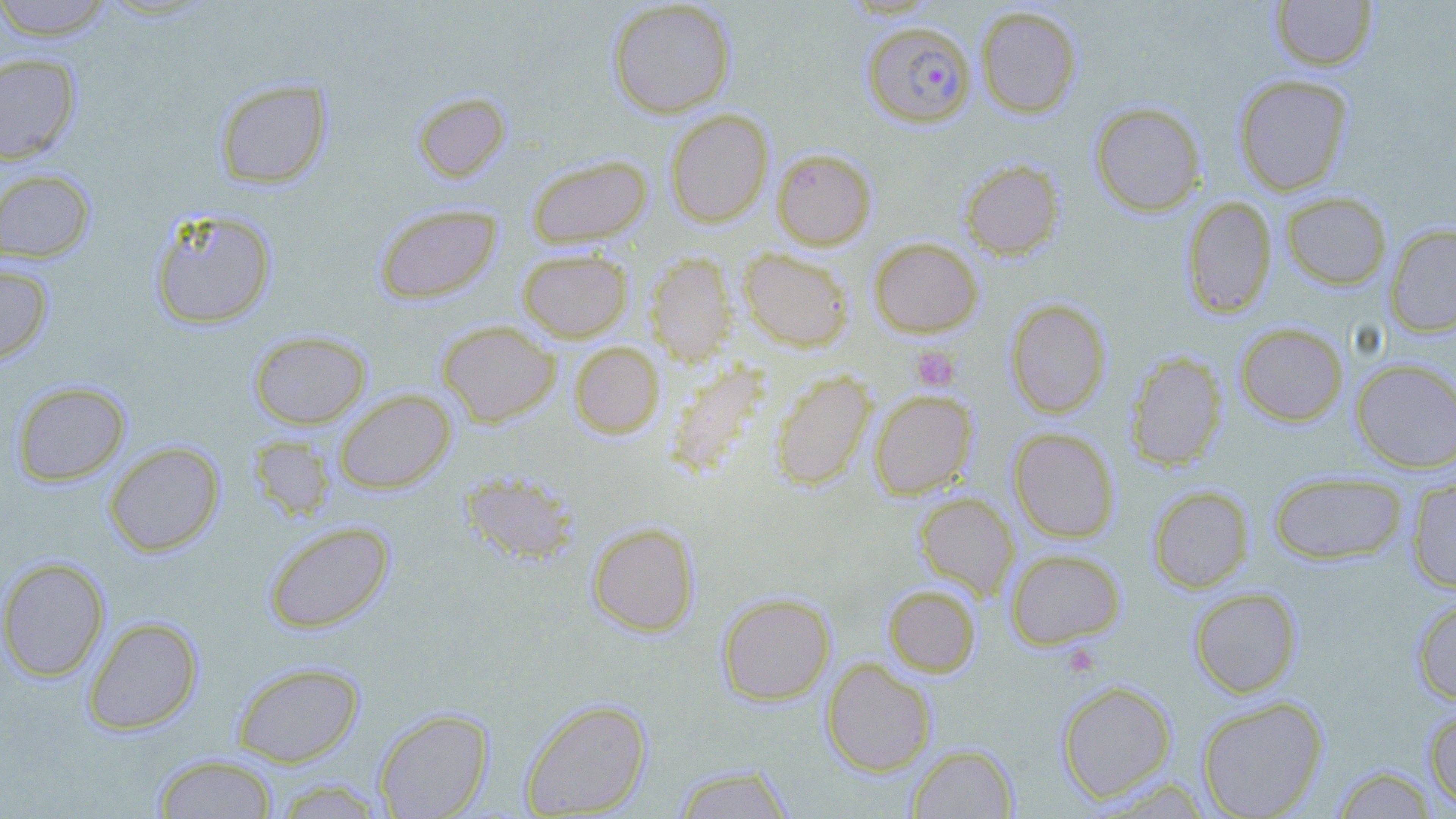

slide_level_diagnosis: Plasmodium falciparum
stain: May-Grünwald-Giemsa
plasmodium_falciparum_infected_red_blood_cell_locations: 'approximate bounding boxes as (x1, y1, x2, y2) in pixels: (862, 21, 976, 127)'
magnification: 1000x
modality: light microscopy
platelet_locations: 'approximate bounding boxes as (x1, y1, x2, y2) in pixels: (911, 345, 961, 393)'
uninfected_red_blood_cell_locations: 'approximate bounding boxes as (x1, y1, x2, y2) in pixels: (0, 0, 116, 41), (1270, 0, 1377, 72), (607, 1, 736, 118), (975, 5, 1082, 118), (0, 53, 81, 164), (1232, 74, 1353, 196), (213, 78, 332, 189), (412, 91, 511, 182), (1089, 101, 1206, 217), (664, 109, 774, 228), (772, 148, 876, 250), (526, 154, 652, 248), (959, 158, 1065, 260), (0, 169, 95, 264), (1281, 191, 1391, 290), (1181, 197, 1276, 318), (373, 203, 502, 305), (149, 208, 277, 329), (1385, 223, 1456, 337), (868, 237, 983, 337), (738, 248, 854, 352), (517, 249, 633, 342), (646, 253, 736, 365), (0, 263, 53, 364), (1005, 298, 1111, 418), (436, 320, 560, 427), (1235, 322, 1348, 426), (248, 330, 371, 429), (569, 342, 665, 439), (1125, 351, 1227, 471), (1351, 358, 1456, 473), (665, 359, 772, 480), (770, 370, 875, 490), (12, 381, 130, 487), (334, 389, 456, 494), (868, 389, 977, 499), (1008, 428, 1120, 542), (248, 435, 336, 521), (103, 441, 224, 557), (461, 471, 580, 565), (1268, 471, 1407, 565), (1406, 478, 1456, 592), (1148, 486, 1253, 593), (914, 491, 1019, 600), (263, 521, 395, 633), (586, 521, 700, 637), (1005, 548, 1126, 649), (0, 556, 110, 682), (883, 584, 981, 677), (1188, 587, 1302, 698), (717, 592, 835, 705), (1411, 596, 1456, 705), (82, 616, 203, 735), (821, 657, 937, 777), (231, 661, 364, 766), (1056, 679, 1177, 803), (1196, 695, 1328, 819), (520, 698, 652, 817), (1424, 706, 1456, 811), (373, 707, 493, 819), (907, 744, 1018, 818), (153, 754, 278, 818), (672, 764, 796, 818), (1331, 765, 1437, 818), (271, 778, 387, 818)'
field_of_view: one of a larger specimen
preparation: thin blood smear
image_size: 1456×819 pixels